Classify the preparation.
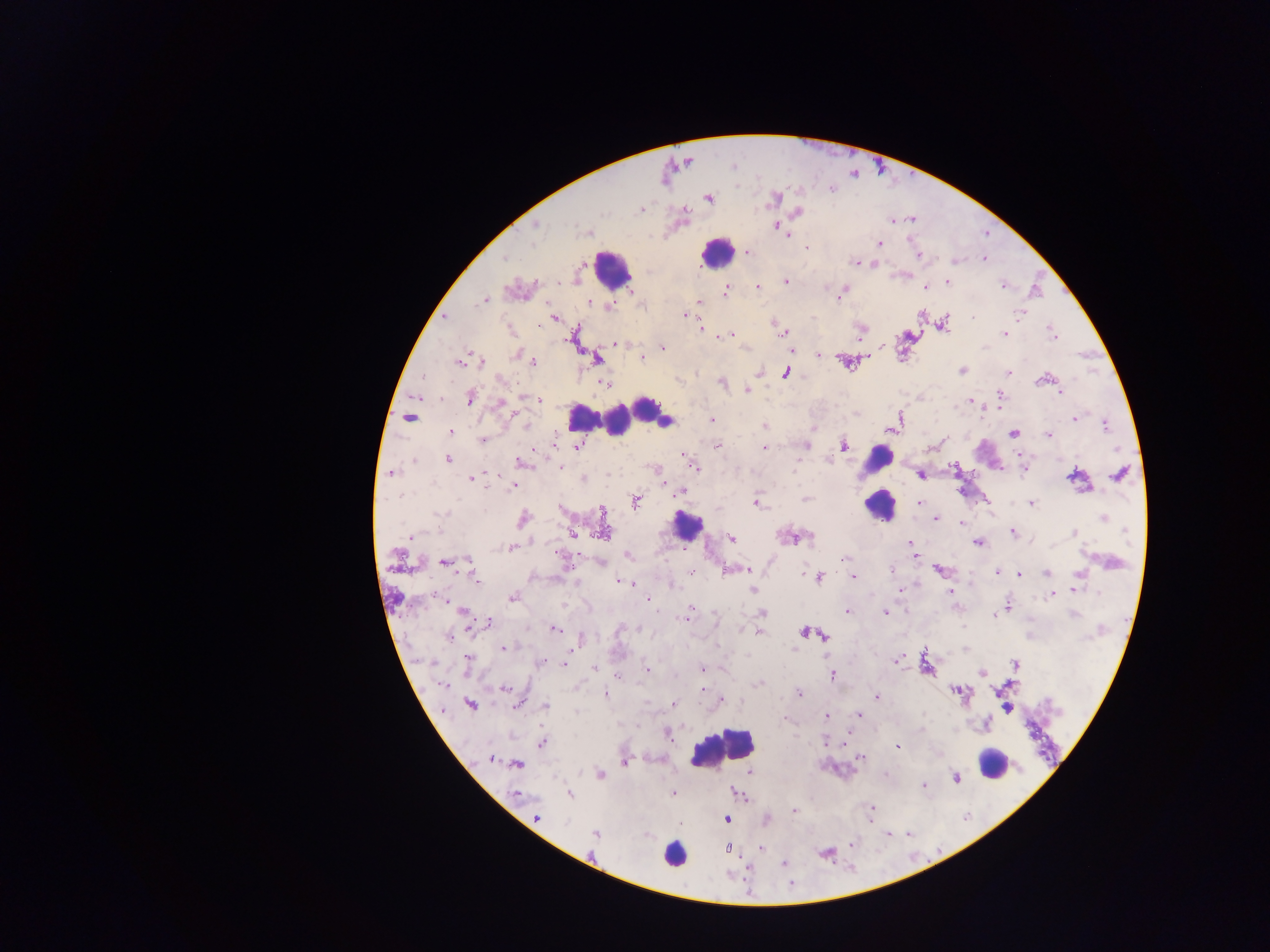

This is a thick smear.

Approximate centers as (x, y) in pixels.
Summary:
  - Leukocyte locations: (713, 256), (618, 272), (658, 409), (596, 418), (877, 458), (878, 509), (688, 525), (721, 748), (992, 768), (671, 856)
  - Plasmodium parasite locations (subset; some below the resolvable size): (775, 197), (708, 198), (798, 213), (912, 220), (773, 222), (537, 225), (775, 226), (588, 233), (790, 234), (877, 244), (747, 251), (987, 257), (504, 258), (983, 258), (856, 262), (955, 262), (877, 266), (785, 280), (948, 281), (1003, 286), (727, 288), (757, 288), (925, 289), (842, 294), (838, 298), (485, 300), (699, 302), (593, 305), (607, 307), (686, 314), (922, 314), (1019, 314), (446, 317), (554, 317), (971, 317), (775, 327), (701, 328), (779, 333), (732, 334), (785, 334), (1004, 335), (1053, 336), (717, 337), (725, 337), (615, 345), (662, 347), (985, 348), (818, 354), (642, 359), (481, 360), (459, 361), (534, 361), (596, 361), (963, 370), (1008, 372), (785, 375), (424, 377), (722, 382), (605, 384), (746, 392), (1059, 392), (1001, 394), (521, 397), (469, 398), (533, 399), (539, 400), (499, 401), (975, 402), (970, 403), (988, 409), (900, 418), (1073, 418), (711, 419), (525, 423), (1105, 424), (887, 430), (448, 433), (1049, 433), (1012, 434), (482, 439), (717, 446), (574, 447), (806, 447), (845, 447), (765, 448), (1117, 449), (533, 450), (684, 455), (1019, 456), (1022, 458), (448, 460), (688, 460), (827, 461), (518, 462), (560, 466), (954, 466), (694, 467), (1023, 472), (389, 473), (606, 473), (921, 476), (471, 480), (512, 487), (489, 488), (681, 491), (400, 495), (806, 498), (919, 503), (756, 504), (1030, 504), (988, 505), (992, 509), (443, 514), (1104, 518), (523, 519), (936, 520), (962, 522), (1012, 532), (1128, 532), (1075, 533), (573, 534), (409, 536), (808, 536), (406, 537), (732, 538), (911, 544), (978, 544), (511, 548), (466, 560), (846, 560), (745, 568), (892, 568), (938, 569), (996, 572), (691, 574), (1020, 575), (1046, 575), (820, 577), (852, 578), (476, 581), (574, 583), (617, 583), (754, 590), (898, 590), (1079, 590), (948, 591), (1074, 591), (1098, 591), (1055, 595), (1050, 597), (513, 599), (647, 599), (445, 600), (447, 602), (1009, 603), (689, 607), (462, 612), (656, 612), (846, 612), (762, 613), (883, 613), (685, 614), (994, 615), (1073, 615), (685, 620), (488, 623), (555, 629), (638, 629), (757, 631), (803, 632), (823, 636), (447, 638), (504, 648), (466, 658), (892, 660), (564, 662), (897, 662), (429, 663), (541, 663), (595, 669), (704, 669), (646, 671), (981, 673), (831, 675), (444, 687), (506, 687), (703, 688), (798, 693), (607, 694), (876, 695), (721, 701), (674, 703), (545, 705), (517, 707), (574, 711), (857, 715), (826, 717), (669, 734), (825, 741), (541, 743), (898, 748), (491, 758), (860, 758), (623, 763), (517, 766), (600, 774), (749, 774), (956, 778), (672, 793), (793, 813), (539, 818), (725, 818), (727, 820), (594, 834), (852, 844), (760, 847), (729, 849), (781, 865)
  - Capture: mobile-phone photograph through a microscope
  - Country: Ghana
  - Image size: 1270×952 pixels
  - Field of view: single